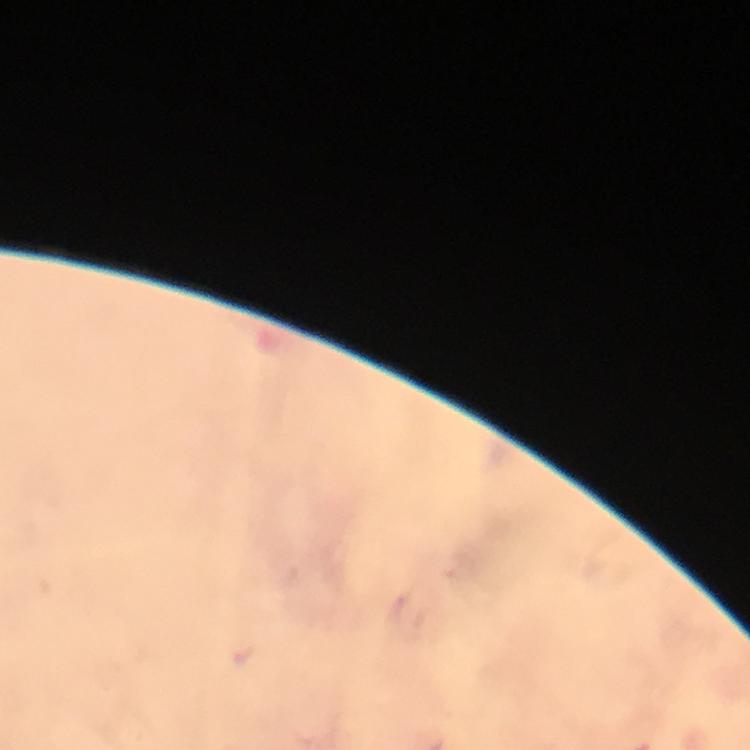
Approximate object centers, in pixels from the top-left corner. Plasmodium parasite locations: (x=242, y=656). Giemsa stain. Cropped region of a single field of view. At 100x magnification. Immersion oil applied. From a malaria diagnostic workup. Image is 750×750 pixels. Thick smear. Smartphone photograph taken through a microscope.